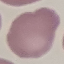

result: no malaria parasites detected
image_type: automatically extracted cell patch, resized to 64 × 64 pixels
preparation: thin smear
stain: Giemsa
capture: smartphone through the microscope eyepiece